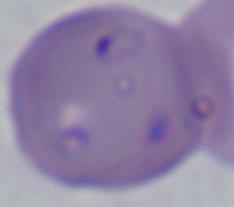 Micrograph. Captured at 1000x magnification. A Babesia parasite is shown.